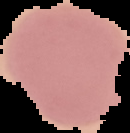

From a thin blood smear. Segmented cell region on a black background. Image is 130×133 pixels. Result: negative for Plasmodium parasites.